Assess this cell for malaria.
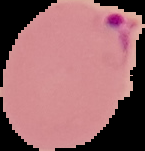

It is parasitized.

Image is 145×151 pixels. From a thin blood smear. Cell region segmented out of the field of view; the surrounding area is masked to black.